Identify the cell.
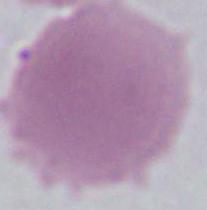
An erythrocyte.

Summary:
  - Magnification: 1000x
  - Modality: photomicrograph